Locate every blood parasite and identify its species.
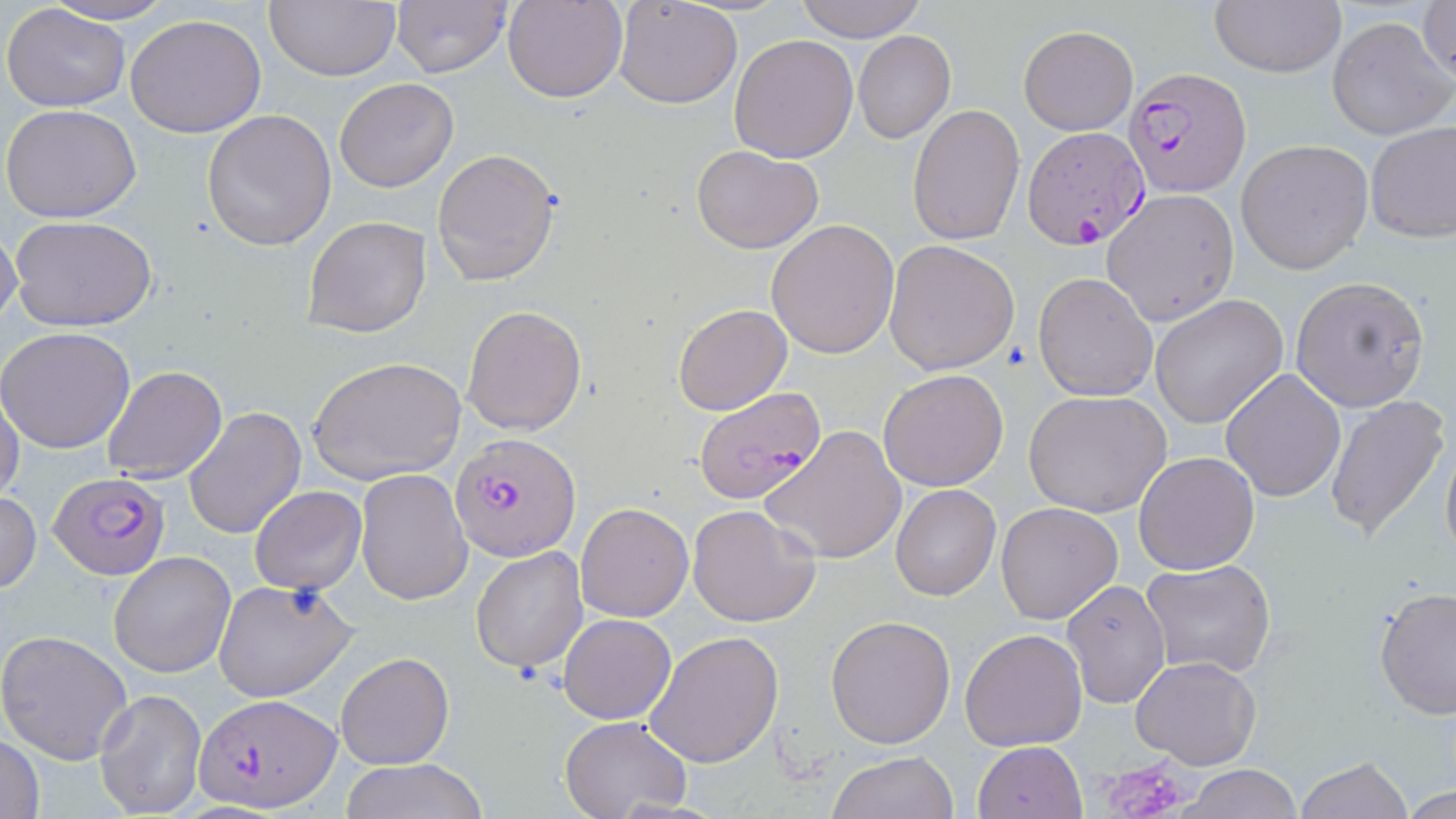

Approximate bounding boxes as named x1/y1/x2/y2 corners in pixels.
Plasmodium falciparum-infected red blood cells: (x1=1124, y1=68, x2=1250, y2=198), (x1=1022, y1=128, x2=1148, y2=250), (x1=693, y1=386, x2=825, y2=507), (x1=451, y1=433, x2=581, y2=561), (x1=49, y1=471, x2=170, y2=581), (x1=195, y1=692, x2=342, y2=813).
No Plasmodium ovale, Plasmodium malariae, Plasmodium vivax, Babesia divergens, or Trypanosoma brucei observed.

{
  "slide_level_diagnosis": "Plasmodium falciparum",
  "image_size": "1456×819 pixels",
  "preparation": "thin blood film",
  "stain": "May-Grünwald-Giemsa",
  "magnification": "1000x",
  "modality": "light microscopy",
  "uninfected_red_blood_cell_locations": "approximate bounding boxes as named x1/y1/x2/y2 corners in pixels: (x1=42, y1=0, x2=174, y2=26), (x1=267, y1=0, x2=403, y2=81), (x1=503, y1=0, x2=630, y2=103), (x1=614, y1=0, x2=743, y2=108), (x1=792, y1=0, x2=929, y2=42), (x1=1210, y1=0, x2=1347, y2=77), (x1=1418, y1=0, x2=1455, y2=85), (x1=391, y1=1, x2=512, y2=78), (x1=3, y1=4, x2=131, y2=111), (x1=125, y1=14, x2=267, y2=138), (x1=1327, y1=16, x2=1452, y2=141), (x1=1019, y1=26, x2=1138, y2=136), (x1=853, y1=30, x2=957, y2=144), (x1=729, y1=32, x2=858, y2=162), (x1=334, y1=77, x2=459, y2=192), (x1=2, y1=104, x2=143, y2=224), (x1=907, y1=105, x2=1025, y2=245), (x1=201, y1=109, x2=337, y2=250), (x1=1366, y1=120, x2=1456, y2=242), (x1=1235, y1=139, x2=1374, y2=274), (x1=692, y1=144, x2=824, y2=254), (x1=433, y1=149, x2=561, y2=287), (x1=1103, y1=189, x2=1240, y2=326), (x1=301, y1=215, x2=431, y2=340), (x1=12, y1=216, x2=156, y2=332), (x1=766, y1=219, x2=899, y2=359), (x1=0, y1=225, x2=23, y2=337), (x1=883, y1=239, x2=1021, y2=374), (x1=1032, y1=272, x2=1158, y2=402), (x1=1289, y1=275, x2=1430, y2=413), (x1=1150, y1=294, x2=1288, y2=430), (x1=673, y1=303, x2=792, y2=415), (x1=462, y1=306, x2=586, y2=436), (x1=0, y1=326, x2=135, y2=452), (x1=309, y1=355, x2=467, y2=486), (x1=102, y1=364, x2=228, y2=485), (x1=1220, y1=367, x2=1347, y2=502), (x1=879, y1=368, x2=1010, y2=492), (x1=1025, y1=389, x2=1174, y2=517), (x1=0, y1=392, x2=24, y2=506), (x1=1325, y1=392, x2=1451, y2=543), (x1=184, y1=407, x2=306, y2=540), (x1=761, y1=425, x2=908, y2=565), (x1=1440, y1=431, x2=1456, y2=568), (x1=1132, y1=451, x2=1259, y2=575), (x1=354, y1=470, x2=472, y2=605), (x1=891, y1=483, x2=1000, y2=600), (x1=249, y1=485, x2=366, y2=595), (x1=0, y1=489, x2=41, y2=594), (x1=574, y1=501, x2=693, y2=621), (x1=995, y1=501, x2=1124, y2=624), (x1=687, y1=504, x2=822, y2=629), (x1=471, y1=546, x2=589, y2=674), (x1=109, y1=551, x2=237, y2=677), (x1=1140, y1=559, x2=1277, y2=679), (x1=213, y1=578, x2=359, y2=703), (x1=1060, y1=579, x2=1171, y2=709), (x1=1374, y1=586, x2=1456, y2=719), (x1=558, y1=612, x2=677, y2=724), (x1=826, y1=616, x2=955, y2=748), (x1=959, y1=628, x2=1088, y2=751), (x1=0, y1=629, x2=134, y2=764), (x1=645, y1=630, x2=784, y2=769), (x1=335, y1=650, x2=454, y2=770), (x1=1129, y1=657, x2=1260, y2=770), (x1=93, y1=687, x2=207, y2=818), (x1=559, y1=716, x2=693, y2=819), (x1=1, y1=734, x2=46, y2=818), (x1=973, y1=740, x2=1088, y2=819), (x1=828, y1=750, x2=958, y2=819), (x1=1295, y1=757, x2=1414, y2=818), (x1=341, y1=759, x2=488, y2=819), (x1=1180, y1=765, x2=1304, y2=819), (x1=1401, y1=785, x2=1454, y2=818)",
  "field_of_view": "single",
  "platelet_locations": "approximate bounding boxes as named x1/y1/x2/y2 corners in pixels: (x1=1098, y1=758, x2=1190, y2=819)"
}